State the preparation type.
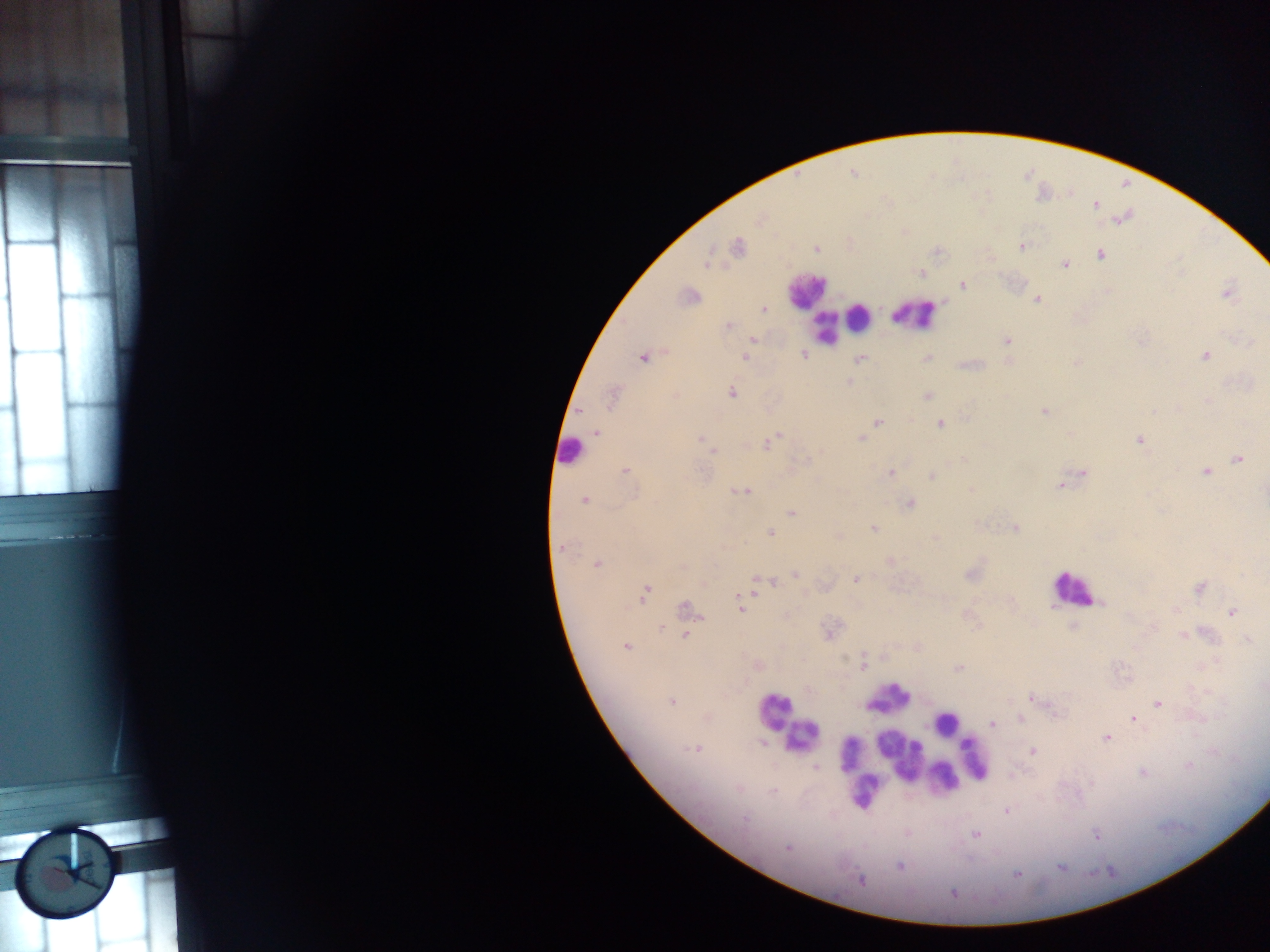
Thick blood smear.

Approximate centers as x y in pixels. Leukocyte locations: 805 290; 914 314; 859 318; 825 326; 571 450; 1073 588; 887 697; 774 710; 946 723; 802 736; 890 746; 904 752; 929 754; 851 756; 974 758; 960 768; 944 776; 863 791. Malaria parasite locations: 853 173; 1095 204; 759 218; 737 247; 1021 247; 816 249; 1100 253; 708 262; 1064 264; 922 273; 963 284; 1106 291; 1226 292; 688 296; 1036 298; 763 309; 728 326; 752 339; 1006 341; 1249 343; 12 352; 805 354; 1204 355; 643 356; 744 357; 926 358; 860 359; 1009 360; 1075 362; 848 381; 1248 385; 732 392; 927 395; 612 398; 1208 401; 1043 410; 877 422; 939 424; 597 432; 777 434; 860 438; 701 439; 1139 440; 766 444; 713 451; 1238 458; 624 470; 1206 471; 890 472; 1082 472; 932 475; 1060 485; 971 489; 741 491; 584 500; 909 503; 791 512; 873 528; 1015 528; 771 533; 837 536; 935 536; 561 547; 890 561; 597 564; 682 566; 794 573; 971 573; 855 579; 758 582; 702 584; 1199 587; 645 591; 740 606; 686 609; 1176 609; 1231 612; 965 614; 660 627; 1073 627; 829 631; 685 635; 1183 635; 1247 640; 625 646; 916 647; 884 655; 863 665; 758 666; 958 668; 1262 686; 1030 698; 671 701; 1157 703; 1019 718; 1133 719; 992 724; 1106 738; 696 748; 1031 750; 815 767; 1186 767; 1141 772; 1006 811; 908 833; 976 834; 1096 835; 788 847; 900 866; 1061 866; 1017 874; 860 880; 953 892. Collected in Ghana. Photographed through a microscope with a mobile-phone camera. Image is 1270×952 pixels. One field of view.